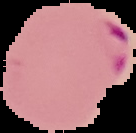
{
  "image_size": "136×133 pixels",
  "preparation": "thin blood film",
  "image_type": "segmented cell region with the area outside set to black",
  "malaria_status": "parasitized"
}